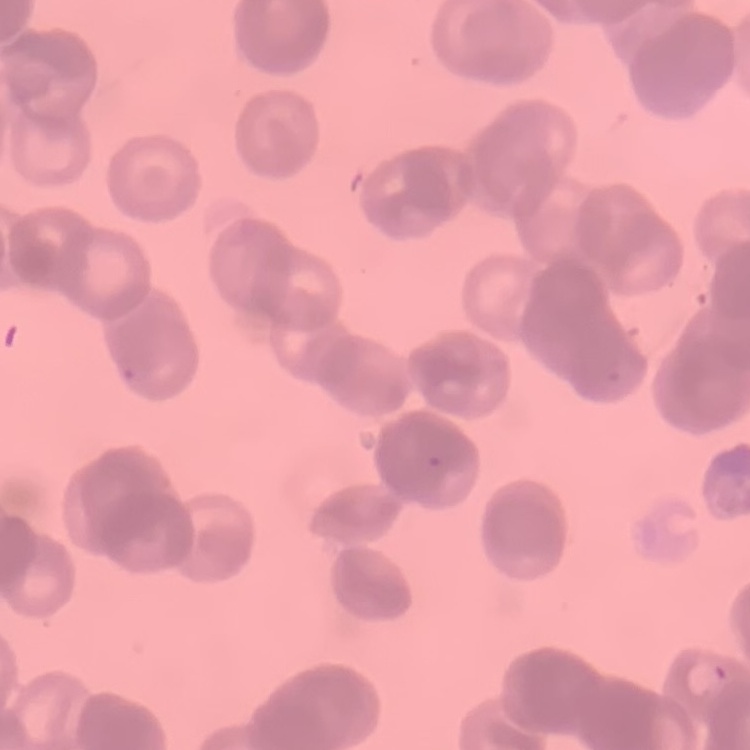
The red blood cells show rouleaux formation. Field's or Giemsa stain. Thin blood film. Square crop of a larger photomicrograph.